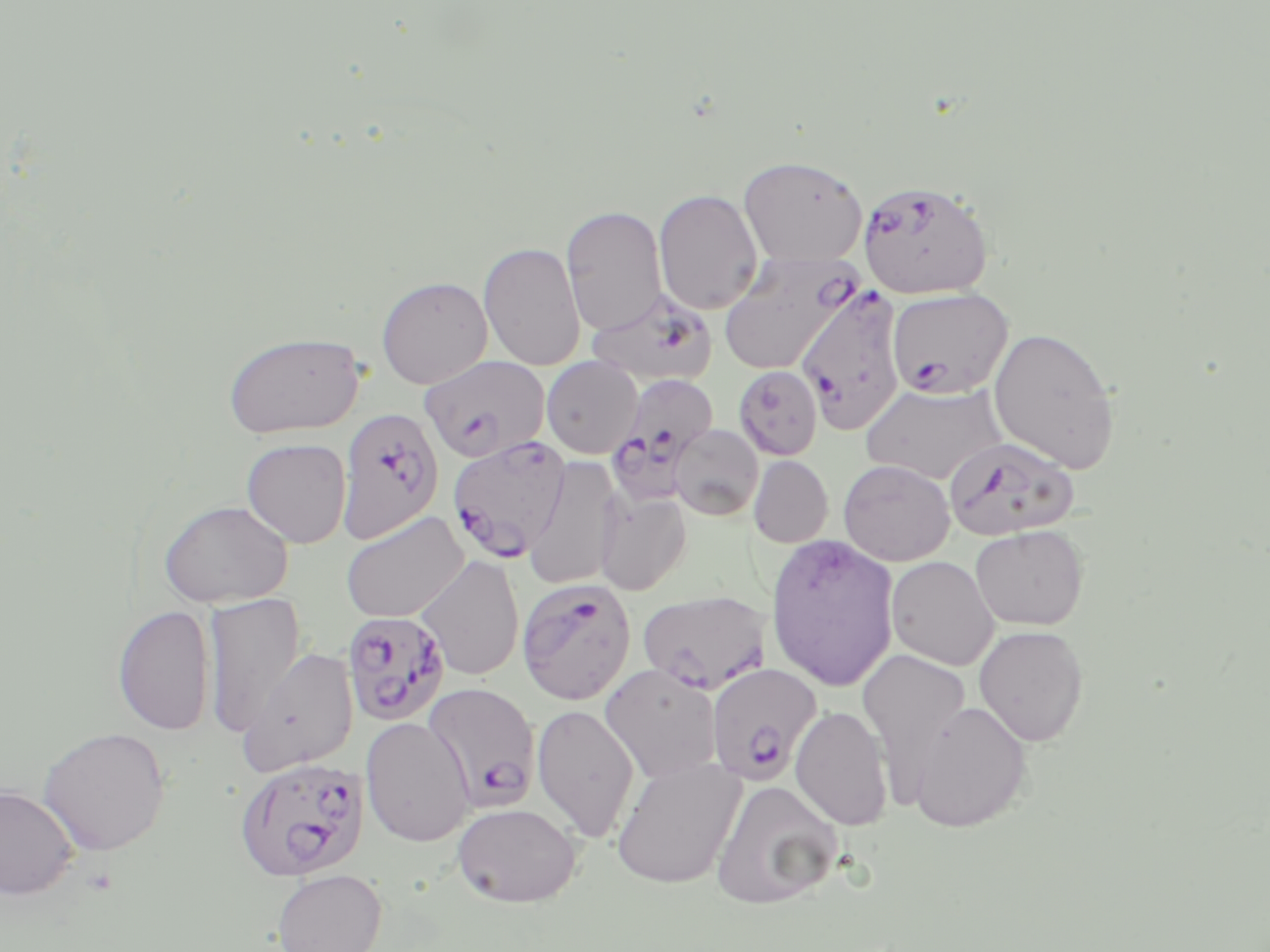
Summary:
  - Coordinate format: approximate bounding boxes as (x1, y1, x2, y2) in pixels
  - Plasmodium falciparum-infected red blood cell locations: (857, 179, 994, 300), (719, 252, 863, 376), (796, 286, 906, 435), (588, 288, 716, 387), (887, 288, 1013, 399), (421, 356, 550, 463), (604, 373, 720, 506), (337, 407, 444, 543), (447, 436, 572, 562), (944, 436, 1080, 541), (516, 577, 636, 706), (638, 589, 771, 694), (342, 611, 450, 725), (706, 663, 822, 785), (424, 682, 540, 810), (234, 756, 369, 881)
  - Uninfected red blood cell locations: (738, 154, 868, 266), (654, 189, 763, 315), (561, 205, 667, 336), (479, 240, 585, 371), (376, 276, 493, 389), (988, 326, 1120, 475), (222, 331, 365, 438), (542, 356, 642, 458), (734, 365, 823, 460), (861, 383, 1006, 485), (670, 424, 763, 521), (241, 438, 352, 548), (523, 455, 624, 591), (748, 455, 833, 548), (838, 459, 955, 566), (596, 491, 691, 595), (157, 499, 293, 608), (340, 511, 468, 623), (970, 524, 1089, 630), (764, 533, 900, 691), (416, 554, 525, 681), (886, 555, 999, 670), (202, 591, 305, 737), (113, 604, 216, 736), (973, 625, 1089, 746), (239, 647, 359, 776), (857, 649, 972, 794), (600, 663, 721, 782), (908, 700, 1032, 832), (532, 703, 639, 843), (790, 704, 893, 830), (360, 716, 475, 847), (38, 726, 171, 856), (611, 755, 746, 890), (710, 779, 843, 909), (0, 784, 80, 900), (452, 802, 582, 908), (272, 869, 387, 952)
  - Slide-level diagnosis: Plasmodium falciparum
  - Magnification: 1000x
  - Modality: optical microscopy
  - Field of view: single
  - Preparation: thin blood smear
  - Image size: 1270×952 pixels
  - Stain: May-Grünwald-Giemsa